Identify the parasite.
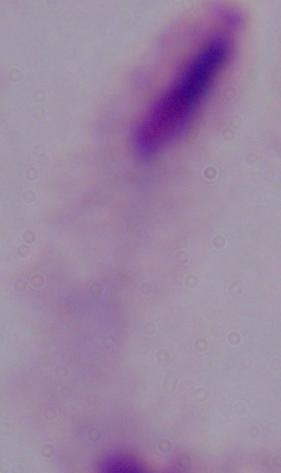
This is a trichomonad.

magnification = 1000x
modality = micrograph